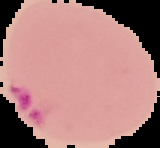
preparation = thin blood smear
result = malaria parasites identified
image type = segmented cell region on a black background
image size = 160×148 pixels